Evaluate for malaria.
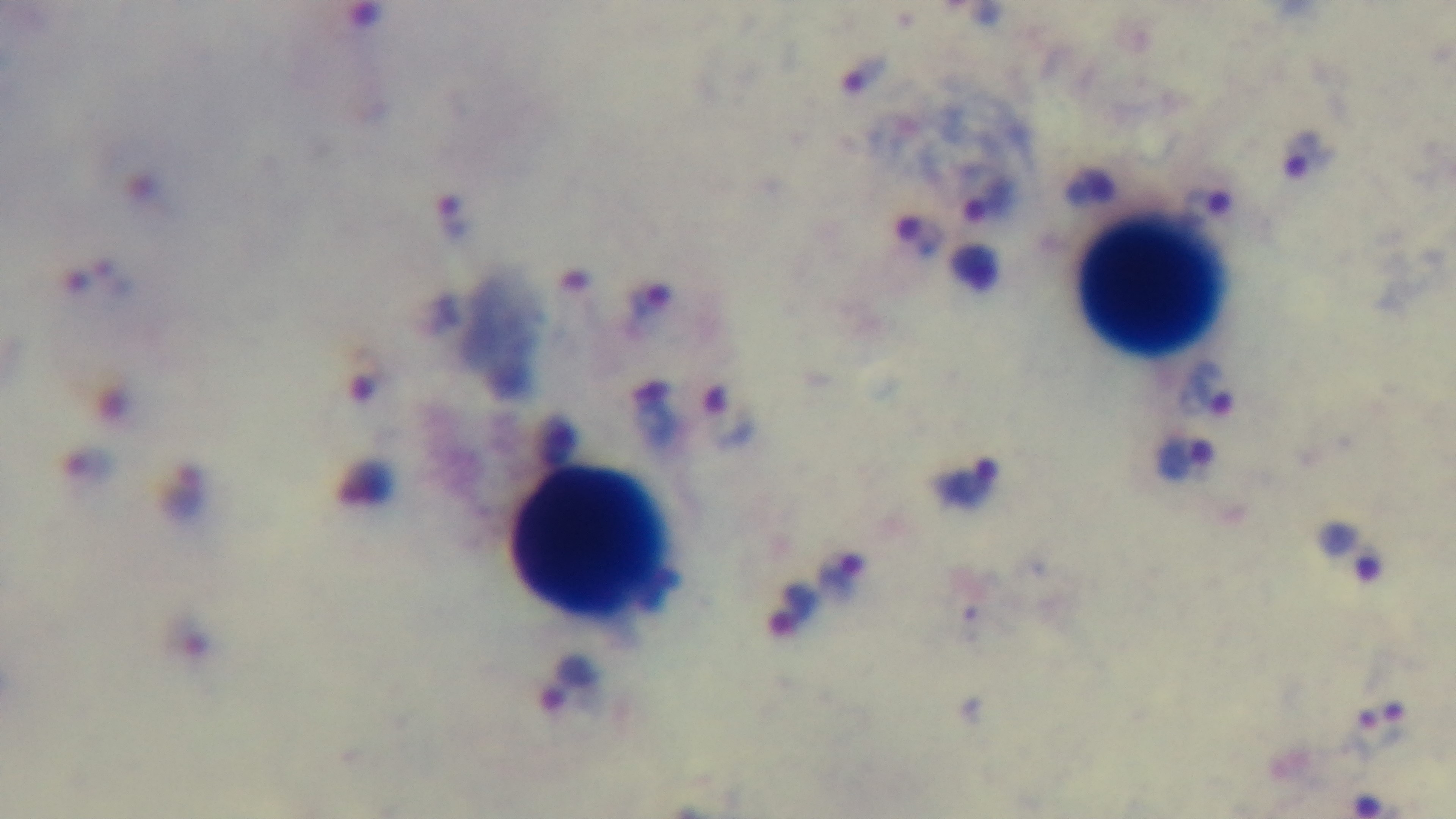
Infected.

Summary:
  - Preparation: thick smear
  - Modality: light microscopy
  - Capture: mounted 4K digital camera
  - Objective: 100x oil immersion
  - Stain: Giemsa
  - Field of view: single